Evaluate for malaria.
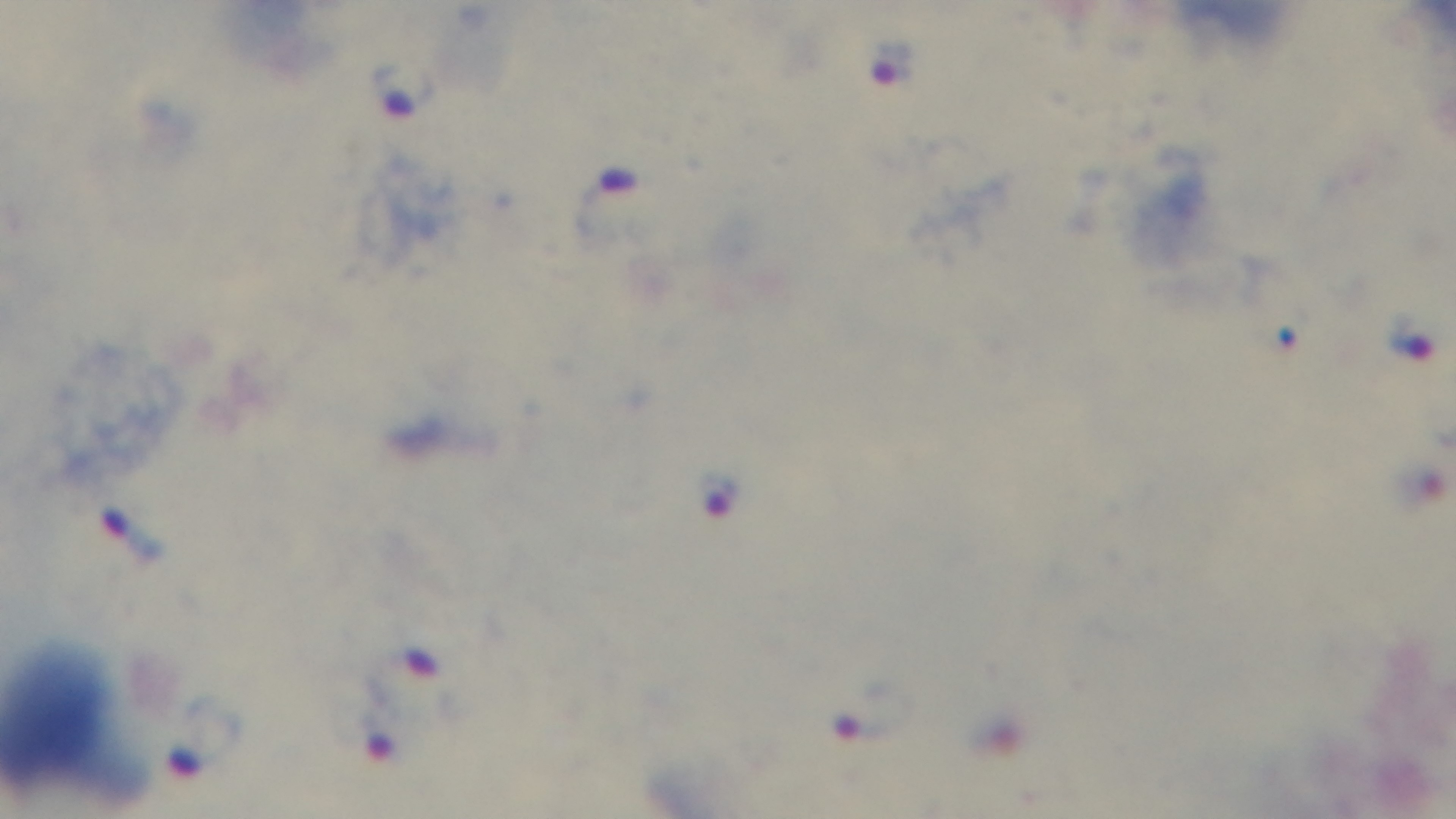

It is infected.

Single field of view. Captured with a mounted 4K digital camera. Giemsa stain. Preparation: thick blood film. 100x oil-immersion objective. Light microscopy.